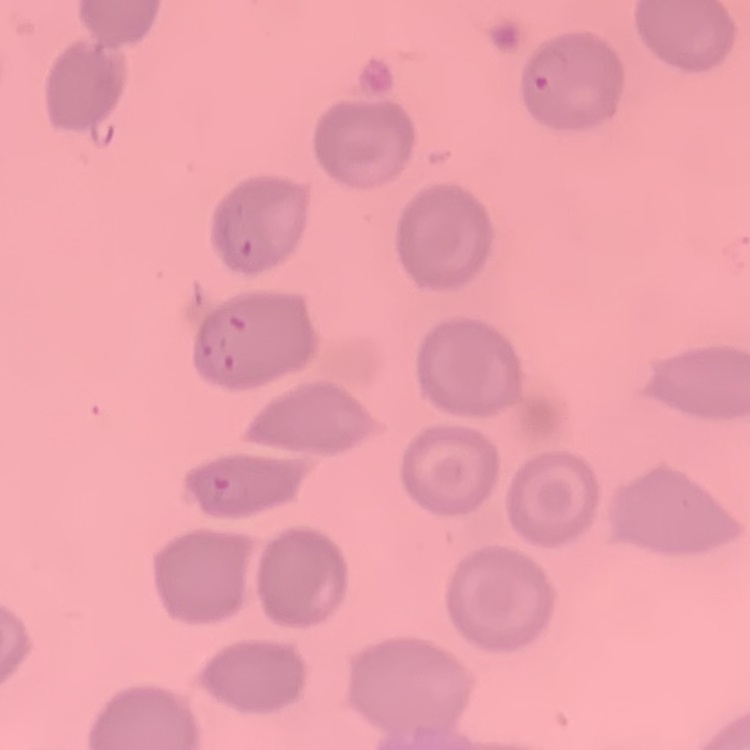
Summary:
  - Erythrocyte morphology: no rouleaux formation
  - Stain: Field's or Giemsa
  - Preparation: thin blood smear
  - Image type: square crop of a larger photomicrograph